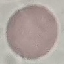

malaria status = uninfected
preparation = thin smear
stain = Giemsa
capture = smartphone camera at the microscope eyepiece
image type = cell patch, automatically extracted from a larger field of view and resized to 64 × 64 pixels